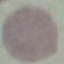

Summary:
  - Malaria status: uninfected
  - Preparation: thin smear
  - Image type: cell patch, automatically extracted from a larger field of view and resized to 64 × 64 pixels
  - Stain: Giemsa
  - Capture: smartphone camera at the microscope eyepiece